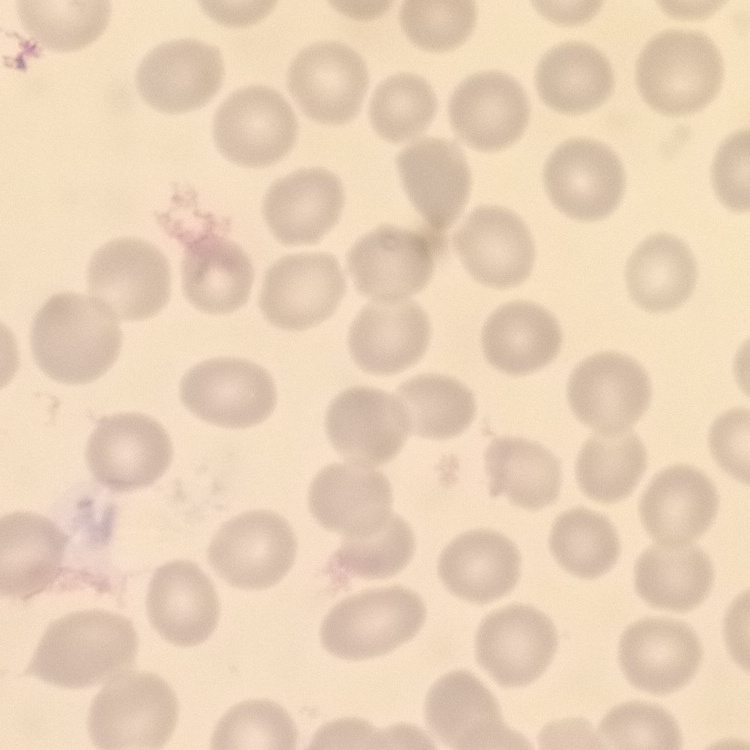

The erythrocytes show no rouleaux formation. One tile cut from a larger photomicrograph. Field's or Giemsa stain. Thin blood film.